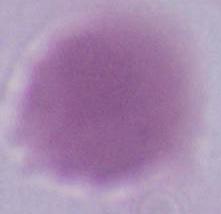

Summary:
  - Magnification: 1000x
  - Modality: photomicrograph
  - Identification: red blood cell